Outline each uninfected red blood cell.
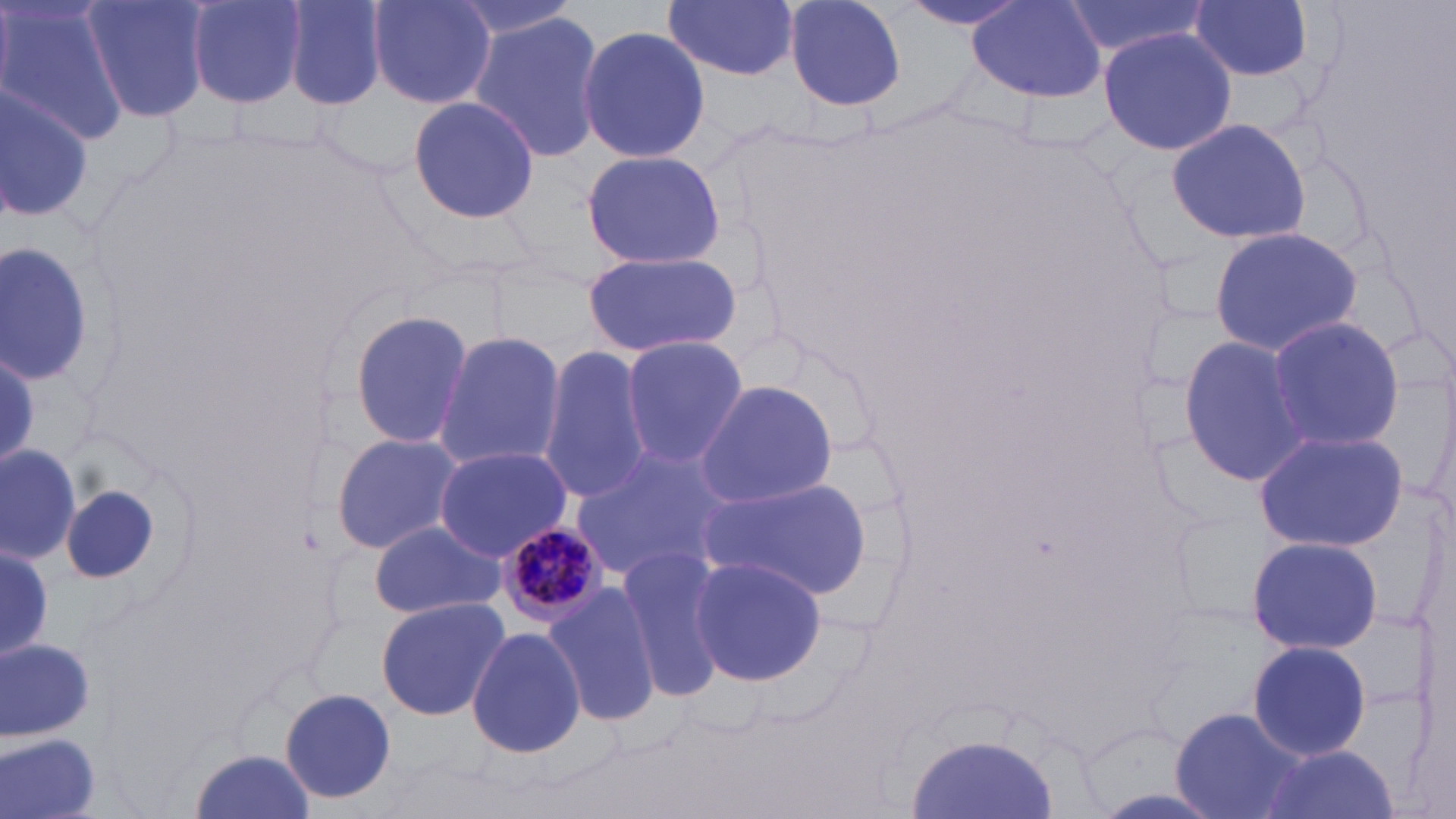

Approximate bounding boxes as (x1, y1, x2, y2) in pixels.
Uninfected red blood cells: (0, 0, 125, 146), (80, 0, 212, 125), (186, 0, 310, 106), (280, 0, 387, 109), (664, 0, 799, 81), (779, 0, 908, 111), (900, 0, 1032, 35), (1060, 0, 1211, 61), (1188, 0, 1317, 82), (366, 1, 495, 110), (966, 2, 1105, 102), (469, 14, 606, 166), (576, 22, 713, 167), (1098, 28, 1239, 158), (0, 85, 96, 222), (405, 94, 541, 225), (1166, 118, 1315, 244), (579, 149, 727, 271), (1207, 226, 1364, 355), (0, 241, 96, 385), (583, 251, 742, 357), (347, 308, 475, 454), (1264, 314, 1404, 455), (434, 332, 566, 469), (1179, 332, 1313, 489), (618, 335, 747, 468), (539, 346, 654, 505), (0, 353, 40, 466), (693, 381, 841, 507), (1253, 428, 1408, 554), (331, 433, 464, 556), (1, 442, 82, 564), (433, 445, 570, 562), (570, 446, 729, 584), (699, 475, 875, 599), (369, 520, 508, 620), (1247, 535, 1386, 655), (0, 545, 54, 660), (617, 547, 730, 697), (687, 556, 828, 685), (543, 583, 660, 726), (374, 597, 510, 721), (466, 627, 587, 759), (1, 638, 96, 744), (1245, 640, 1374, 759), (1205, 659, 1351, 794), (280, 688, 401, 808), (1171, 707, 1305, 819), (904, 731, 1062, 819), (2, 733, 105, 819), (1255, 744, 1397, 819), (188, 748, 317, 819).

slide-level diagnosis = Plasmodium malariae
modality = optical microscopy
image size = 1456×819 pixels
field of view = one of a larger specimen
Plasmodium malariae-infected red blood cell locations = approximate bounding boxes as (x1, y1, x2, y2) in pixels: (495, 521, 607, 629)
magnification = 1000x
preparation = thin blood film
stain = May-Grünwald-Giemsa